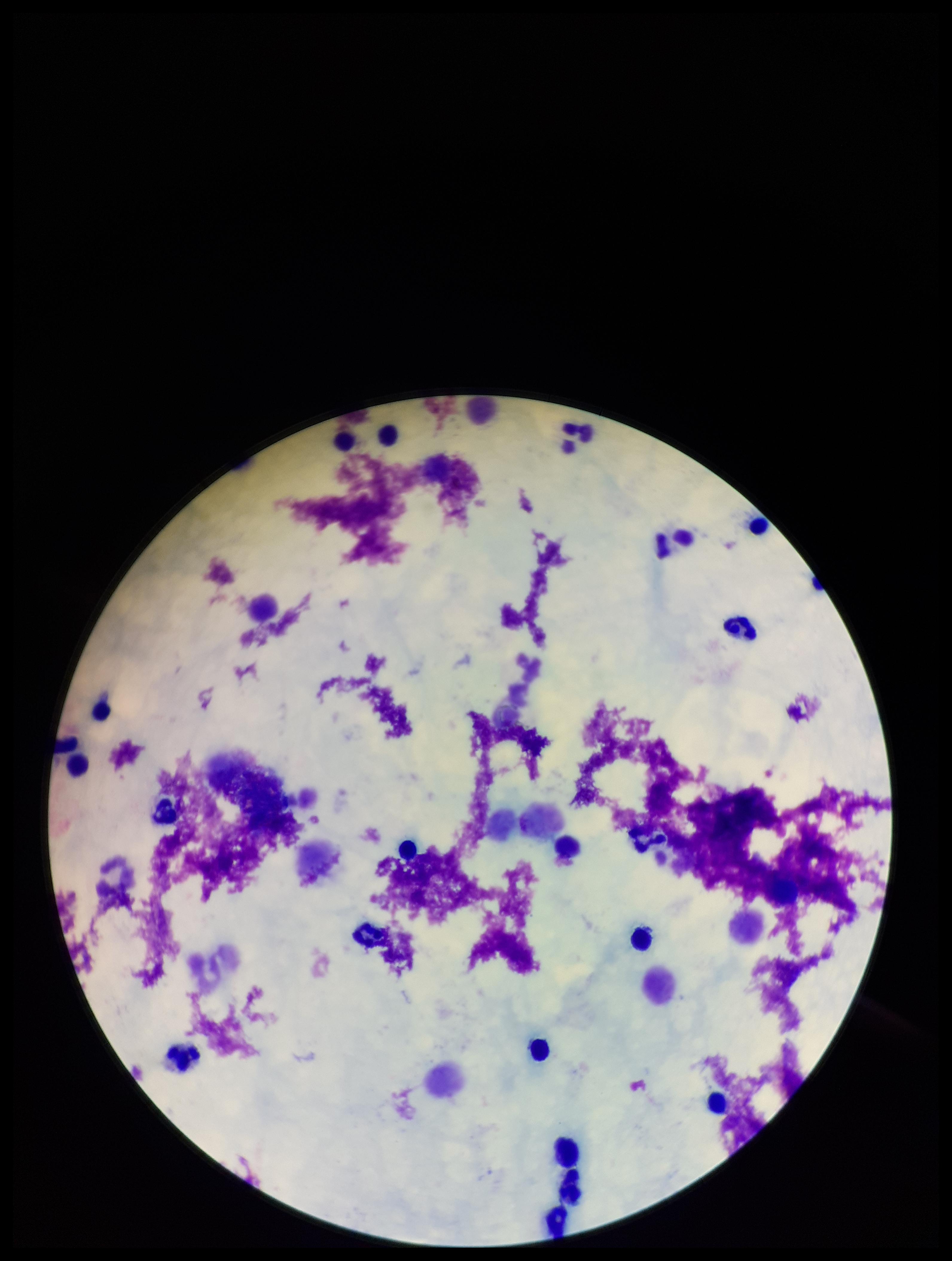

Summary:
  - Plasmodium parasites: none seen
  - Leukocyte count: 22
  - Field of view: single
  - Capture: smartphone photograph through the microscope eyepiece
  - Parasite count: 0
  - Preparation: thick blood smear
  - Patient malaria status: negative
  - Stain: Giemsa
  - Image size: 952×1261 pixels